Name the parasite shown.
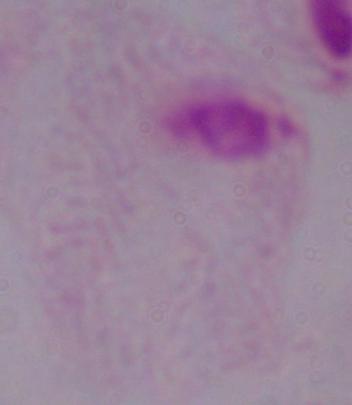
A trichomonad.

{
  "magnification": "1000x",
  "modality": "photomicrograph"
}